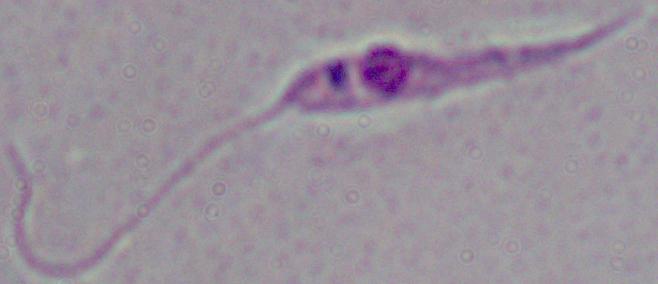
magnification = 1000x
modality = micrograph
identification = Leishmania